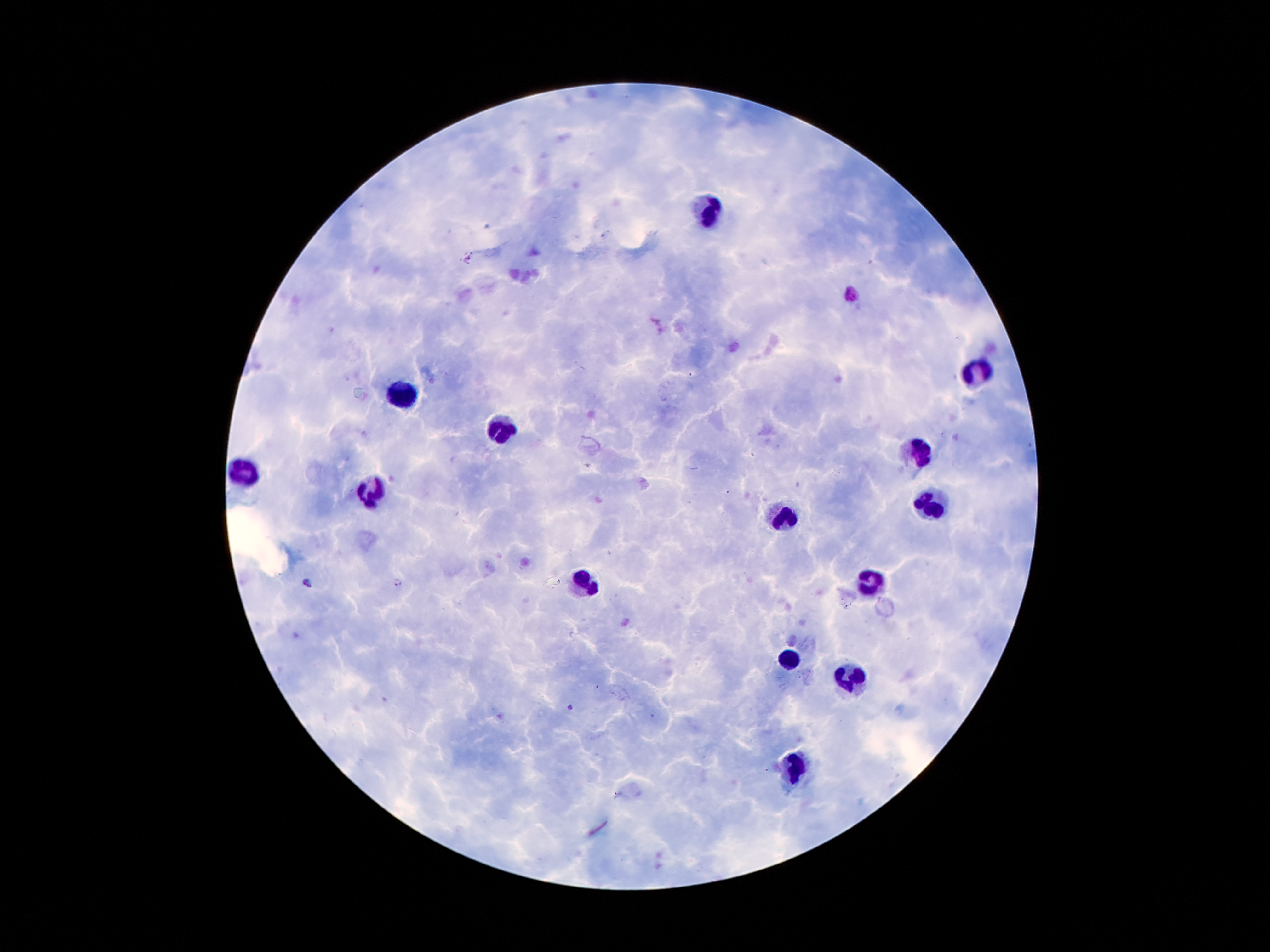

Approximate centers as [x, y] in pixels. Malaria parasite locations: [307, 582], [398, 583], [570, 709]. Leukocyte locations: [708, 210], [979, 371], [400, 396], [502, 432], [919, 453], [241, 476], [372, 492], [933, 505], [783, 519], [592, 578], [870, 578], [790, 660], [851, 678], [795, 771]. Smartphone photograph taken through the microscope eyepiece. Single field of view. Image is 1270×952 pixels. Patient malaria status: infected with Plasmodium falciparum. Thick blood smear. 100x magnification. Giemsa-stained preparation.